Identify the cell.
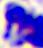
A leukocyte.

modality = micrograph
magnification = 400x